Assess the morphology of the erythrocytes.
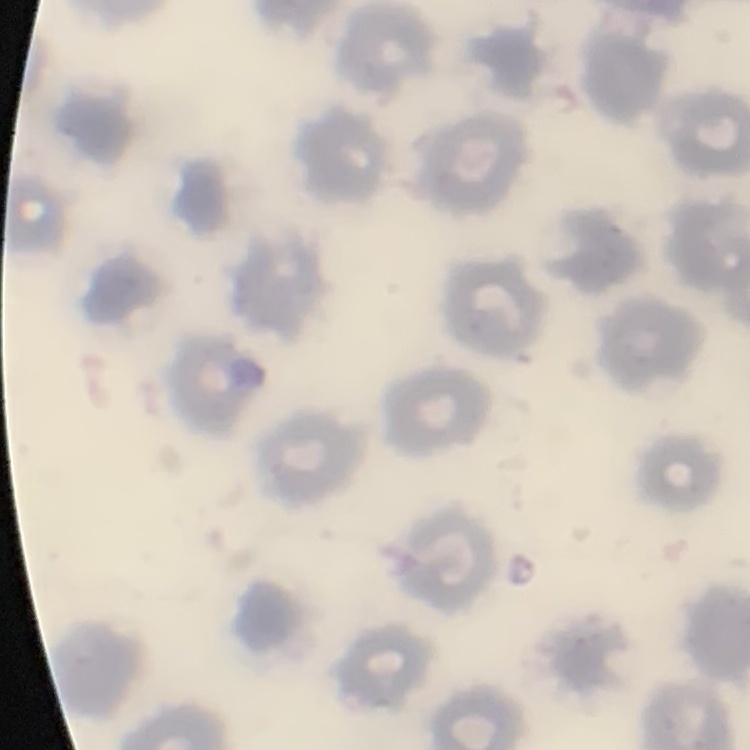
No rouleaux formation.

Square crop of a larger photomicrograph. Field's or Giemsa stain. Thin blood film.